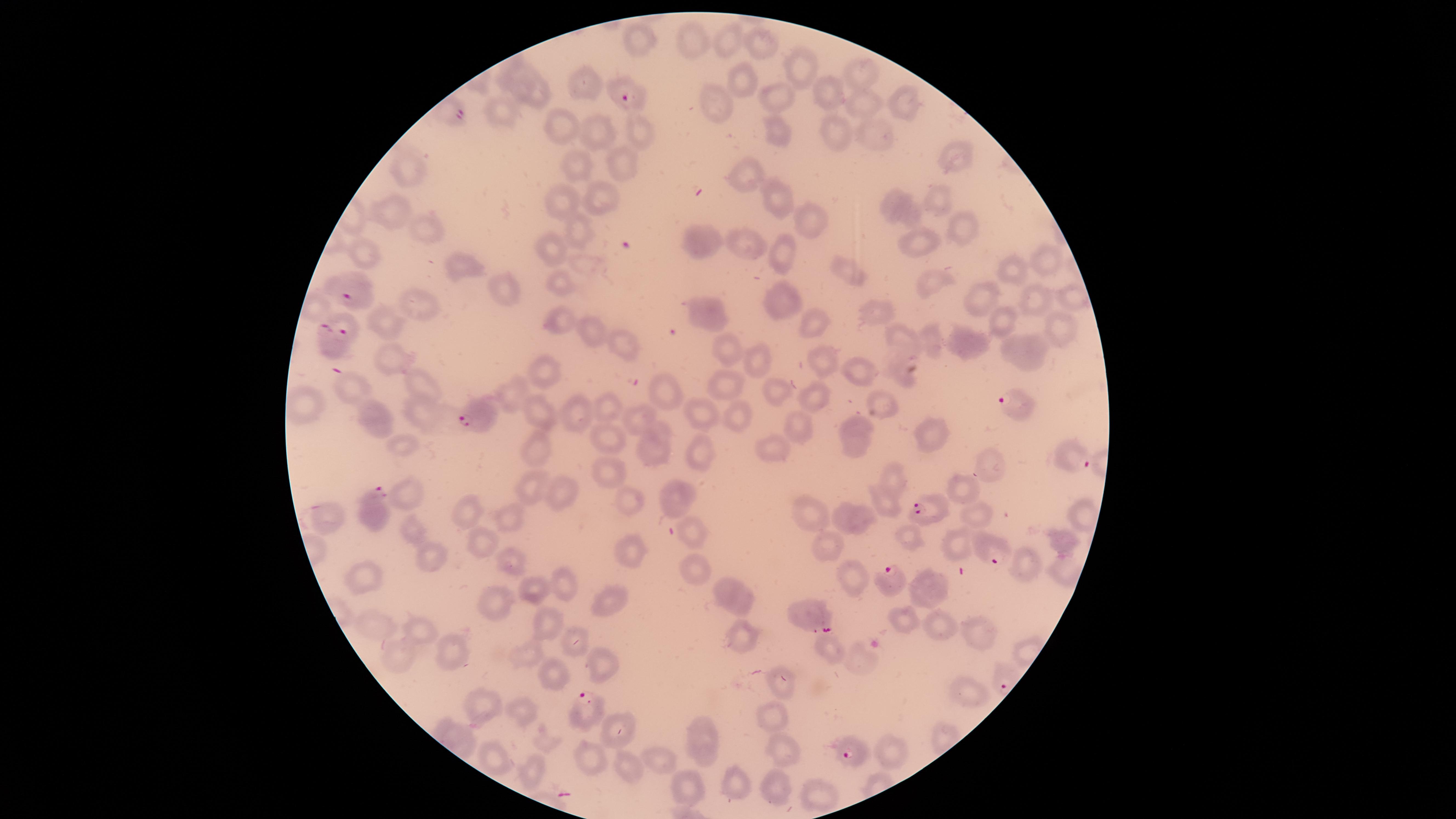

presence: malaria parasites detected
preparation: thin smear of blood
stain: Giemsa
image_size: 1456×819 pixels
uninfected_red_blood_cells: 'approximate marker points as [x, y] in pixels: [696, 38], [727, 38], [642, 40], [762, 45], [793, 62], [505, 69], [863, 74], [741, 75], [581, 81], [825, 82], [775, 91], [539, 93], [722, 100], [901, 101], [862, 102], [500, 112], [780, 124], [560, 128], [871, 129], [598, 130], [640, 130], [841, 130], [955, 156], [617, 161], [417, 164], [580, 168], [743, 175], [774, 194], [941, 195], [597, 196], [564, 201], [903, 205], [394, 212], [806, 218], [574, 224], [957, 226], [428, 227], [706, 240], [912, 243], [749, 246], [779, 252], [557, 253], [369, 254], [1039, 259], [460, 260], [847, 271], [927, 273], [1017, 274], [556, 286], [504, 291], [783, 296], [1073, 296], [980, 297], [1036, 297], [422, 301], [709, 311], [872, 311], [385, 318], [996, 319], [566, 322], [817, 324], [1062, 328], [588, 329], [903, 338], [931, 340], [623, 342], [971, 347], [1020, 352], [386, 354], [730, 355], [819, 359], [761, 363], [546, 367], [854, 368], [725, 379], [421, 382], [352, 390], [777, 391], [514, 392], [664, 394], [812, 397], [874, 399], [310, 403], [607, 407], [733, 409], [694, 411], [538, 412], [429, 415], [581, 415], [641, 417], [858, 421], [381, 422], [798, 428], [661, 431], [928, 433], [608, 436], [858, 444], [775, 445], [695, 448], [649, 450], [533, 451], [989, 464], [613, 472], [892, 476], [530, 489], [559, 490], [965, 490], [410, 497], [680, 497], [630, 499], [884, 502], [469, 510], [811, 511], [975, 513], [334, 515], [841, 515], [1082, 515], [864, 518], [510, 519], [695, 536], [908, 538], [474, 543], [826, 543], [1060, 545], [957, 549], [629, 552], [436, 554], [507, 557], [695, 563], [1025, 566], [1062, 566], [851, 576], [366, 584], [565, 586], [930, 588], [535, 590], [733, 593], [499, 600], [607, 601], [904, 619], [944, 621], [372, 624], [547, 624], [418, 631], [979, 635], [745, 640], [570, 641], [829, 650], [402, 653], [453, 653], [526, 656], [858, 658], [600, 664], [546, 673], [784, 689], [973, 692], [482, 703], [525, 712], [773, 717], [620, 728], [707, 743], [895, 750], [781, 751], [589, 756], [494, 757], [661, 760], [624, 761], [534, 774], [779, 784], [690, 785], [739, 787], [819, 793]'
species: Plasmodium falciparum
field_of_view: single
parasitized_red_blood_cells: 'approximate marker points as [x, y] in pixels: [620, 95], [455, 114], [350, 291], [335, 328], [1008, 407], [476, 414], [1071, 459], [366, 504], [922, 505], [990, 557], [889, 575], [814, 621], [591, 705], [849, 753]'
visible_region: circular
capture: smartphone photograph through the microscope eyepiece